Report the malaria status of this cell.
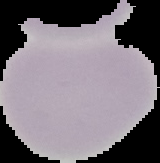

It is uninfected.

Cell region segmented out of the field of view; the surrounding area is masked to black. From a thin blood film. Image is 160×163 pixels.